Mark where platelets are.
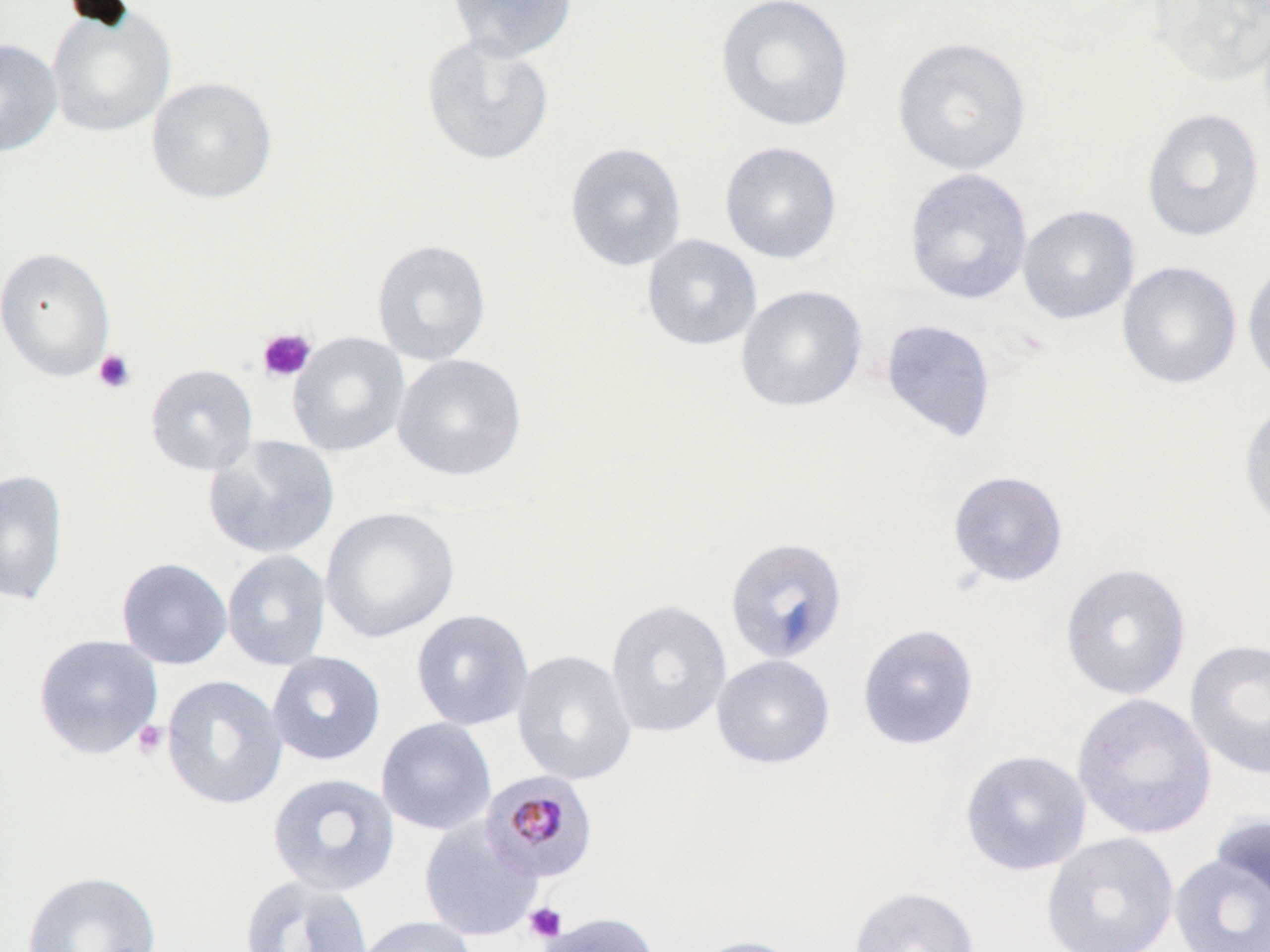

Approximate bounding boxes as (x1, y1, x2, y2) in pixels.
Platelets: (257, 327, 317, 383), (93, 349, 136, 394), (133, 720, 168, 760), (525, 902, 567, 943).

Summary:
  - Uninfected red blood cell locations: (447, 0, 577, 62), (715, 0, 854, 133), (1149, 0, 1270, 86), (45, 5, 177, 138), (421, 33, 555, 166), (891, 35, 1032, 176), (0, 38, 63, 157), (146, 77, 276, 203), (1140, 107, 1265, 243), (719, 140, 842, 264), (564, 142, 687, 272), (904, 168, 1033, 305), (1017, 204, 1140, 324), (641, 233, 763, 351), (371, 239, 492, 365), (0, 246, 116, 382), (1242, 258, 1270, 391), (1116, 260, 1242, 389), (735, 283, 868, 413), (880, 319, 996, 443), (287, 330, 411, 458), (391, 353, 527, 482), (145, 364, 258, 475), (1238, 399, 1270, 531), (203, 435, 340, 560), (0, 469, 68, 606), (948, 470, 1068, 586), (320, 506, 459, 643), (725, 536, 849, 664), (222, 549, 332, 671), (116, 557, 233, 670), (1060, 562, 1191, 700), (606, 599, 732, 738), (410, 608, 535, 731), (857, 623, 979, 749), (33, 633, 164, 759), (1185, 639, 1270, 780), (512, 649, 637, 786), (267, 651, 387, 766), (711, 653, 835, 769), (161, 675, 288, 810), (1072, 693, 1217, 840), (376, 717, 497, 836), (959, 749, 1091, 876), (267, 772, 400, 896), (1209, 814, 1270, 911), (418, 817, 543, 942), (1041, 833, 1179, 952), (1169, 852, 1270, 952), (21, 870, 162, 952), (238, 875, 374, 952), (849, 886, 980, 952), (535, 912, 660, 952), (354, 915, 479, 952), (690, 935, 807, 952)
  - Plasmodium malariae-infected red blood cell locations: (480, 771, 599, 884)
  - Slide-level diagnosis: Plasmodium malariae
  - Stain: May-Grünwald-Giemsa
  - Preparation: thin blood smear
  - Magnification: 1000x
  - Field of view: one of a larger specimen
  - Image size: 1270×952 pixels
  - Modality: light microscopy